Locate every blood parasite and identify its species.
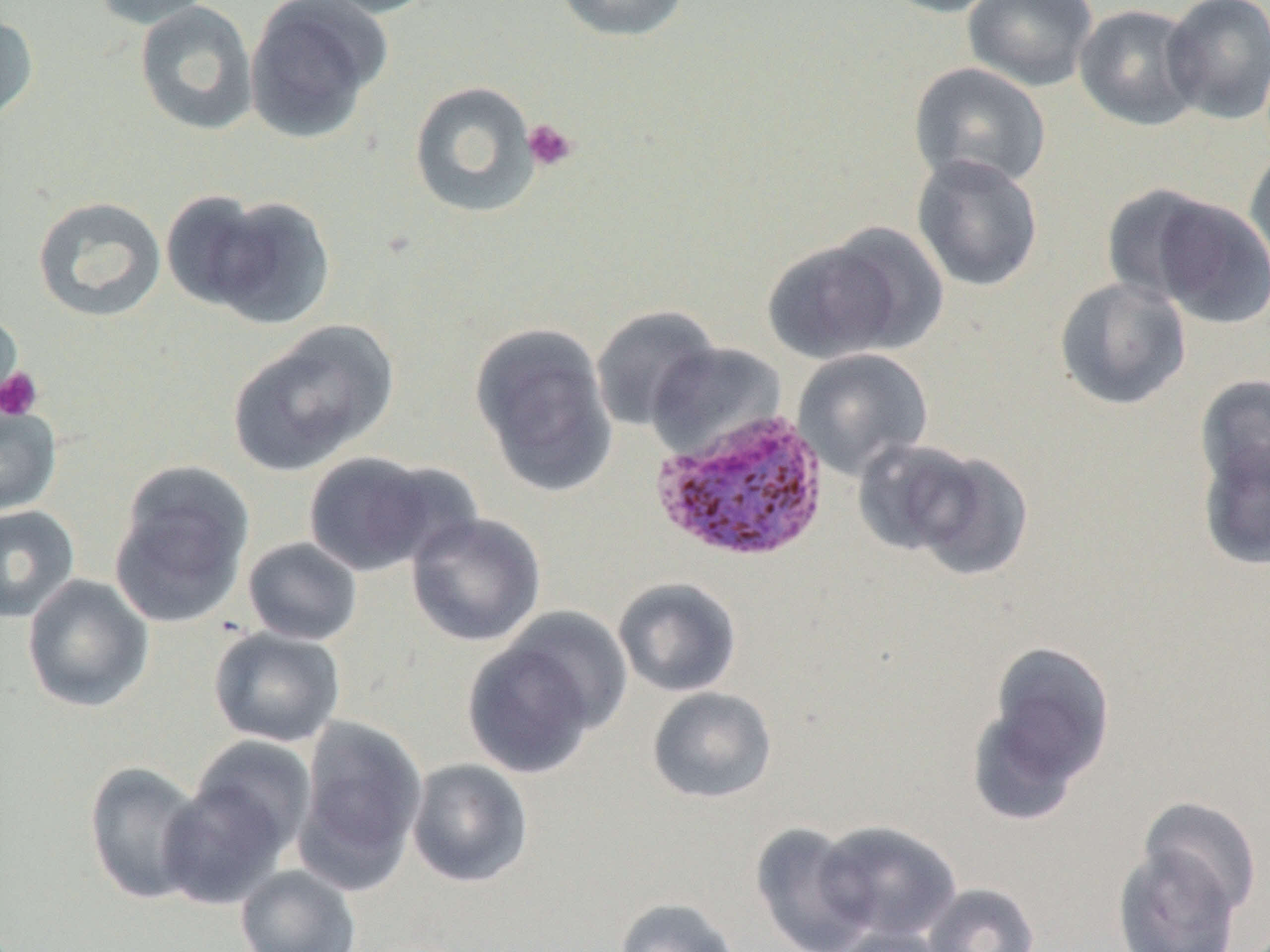
Approximate bounding boxes as (x1,y1)-(x2,y2) corner pairs in pixels.
Plasmodium ovale-infected red blood cells: (651,407)-(833,564).
No Plasmodium falciparum, Plasmodium malariae, Plasmodium vivax, Babesia divergens, or Trypanosoma brucei observed.

Uninfected red blood cell locations: (89,0)-(219,30), (244,0)-(390,143), (310,0)-(444,18), (555,0)-(691,43), (875,0)-(1009,18), (963,0)-(1098,92), (1161,0)-(1270,124), (134,1)-(258,137), (1074,3)-(1205,131), (0,11)-(39,126), (909,62)-(1052,191), (408,80)-(541,218), (1244,144)-(1270,278), (911,154)-(1044,292), (1100,184)-(1226,307), (160,189)-(277,315), (1143,192)-(1270,329), (200,194)-(336,329), (32,195)-(167,322), (761,232)-(920,364), (1054,277)-(1192,411), (590,304)-(721,432), (0,308)-(25,412), (469,321)-(619,495), (226,323)-(397,477), (646,341)-(786,461), (792,348)-(933,481), (1195,375)-(1270,502), (0,404)-(62,516), (1196,431)-(1270,572), (863,440)-(1034,579), (302,450)-(452,577), (109,462)-(255,628), (0,504)-(80,624), (406,512)-(547,647), (242,537)-(363,646), (22,574)-(155,713), (613,577)-(742,697), (499,607)-(634,738), (207,627)-(346,748), (462,633)-(601,780), (984,642)-(1114,788), (646,686)-(778,803), (965,690)-(1096,827), (294,715)-(428,891), (186,735)-(318,861), (406,758)-(534,888), (83,760)-(210,905), (158,776)-(293,908), (1138,797)-(1262,917), (814,820)-(962,943), (749,822)-(879,952), (1112,842)-(1244,952), (235,864)-(362,952), (922,882)-(1039,952), (614,897)-(741,952), (827,925)-(955,952). Platelet locations: (522,118)-(579,172), (0,367)-(44,421). Slide-level diagnosis: Plasmodium ovale. Thin blood film. Light microscopy. 1000x magnification. One field of a larger specimen. Image is 1270×952 pixels.